Classify this cell by malaria status.
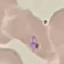
Parasitized.

{
  "image_type": "automatically extracted cell patch, resized to 64 × 64 pixels",
  "stain": "Giemsa",
  "capture": "smartphone through the microscope eyepiece",
  "preparation": "thin blood film"
}